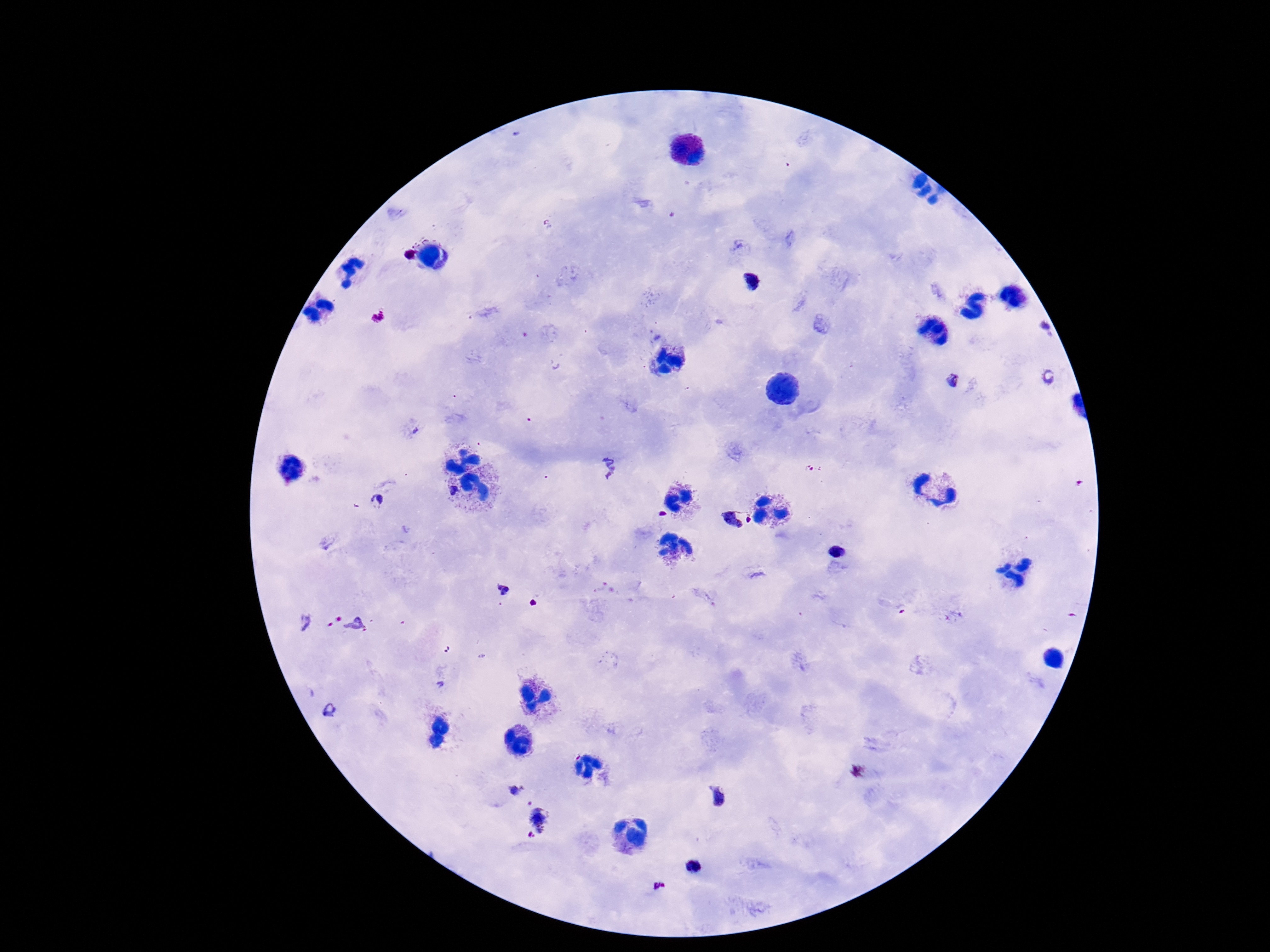

Approximate centers as [x, y] in pixels.
Summary:
  - Plasmodium parasite locations: [410, 253], [754, 281], [378, 316], [1040, 328], [1050, 377], [955, 382], [608, 466], [375, 502], [738, 520], [837, 551], [502, 590], [354, 626], [330, 708], [516, 787], [719, 798], [539, 819], [691, 867], [660, 886]
  - Capture: smartphone camera through the microscope eyepiece
  - Field of view: one from this slide
  - Preparation: thick blood film
  - Image size: 1270×952 pixels
  - Patient malaria status: infected
  - Stain: Giemsa
  - Magnification: 100x